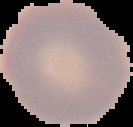

result = negative for Plasmodium parasites
image size = 133×127 pixels
preparation = thin blood smear
image type = cell region segmented out of the field of view; surrounding area masked to black